Assess this cell for malaria.
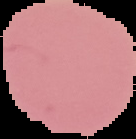

Uninfected.

Image is 136×139 pixels. From a thin blood film. The area outside the segmented cell region is set to black.